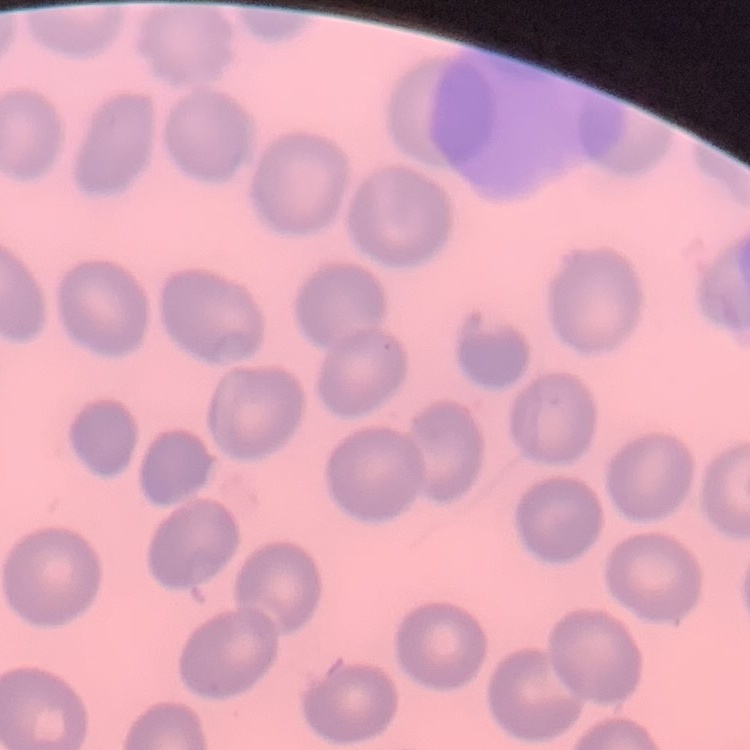

Summary:
  - Red blood cell morphology: no rouleaux formation
  - Stain: Field's or Giemsa
  - Image type: square crop of a larger photomicrograph
  - Preparation: thin peripheral smear